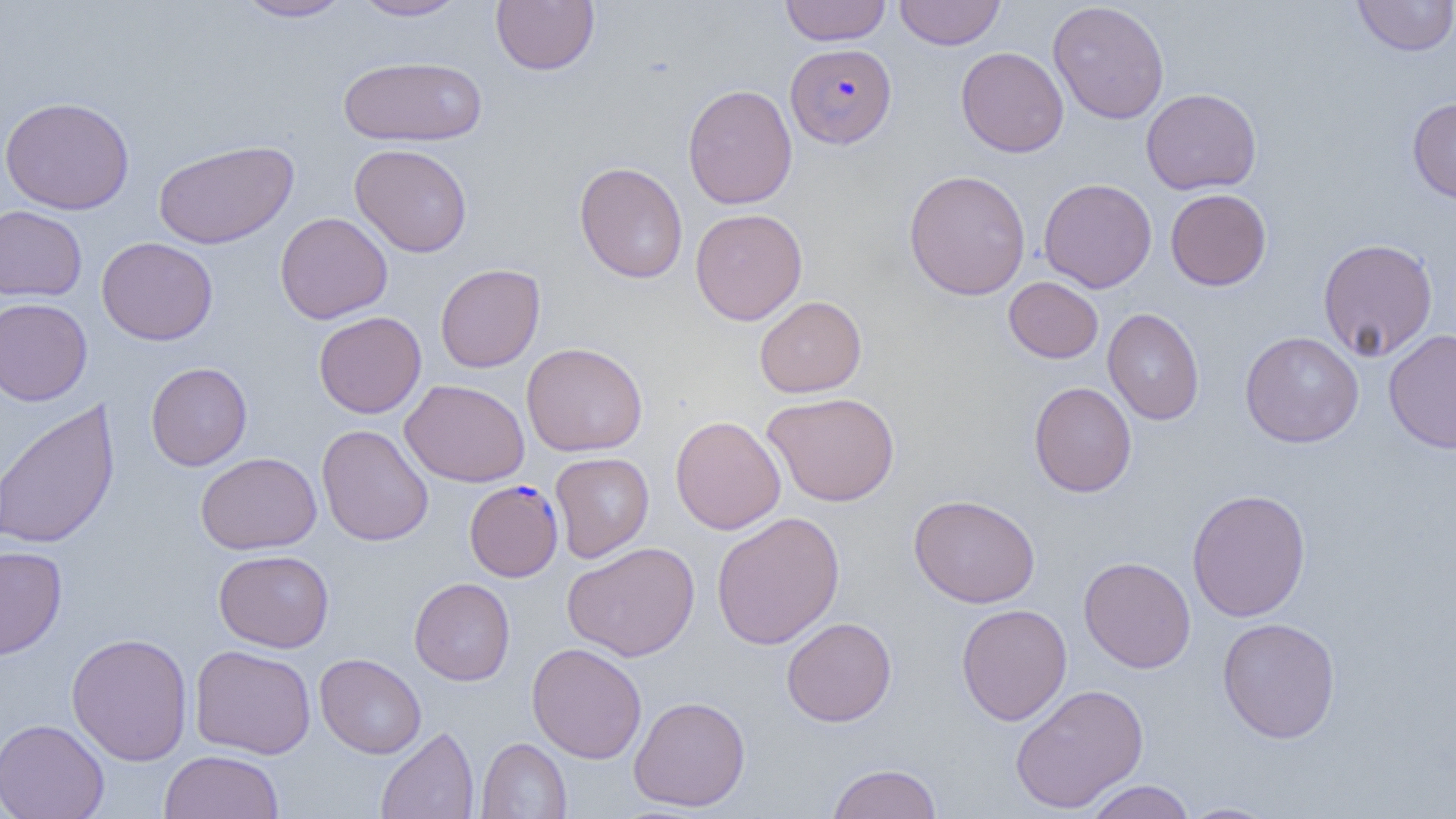

Summary:
  - Coordinate format: approximate bounding boxes as [x1, y1, x2, y2] in pixels
  - Plasmodium falciparum-infected red blood cell locations: [785, 43, 897, 148], [464, 479, 563, 581]
  - Uninfected red blood cell locations: [234, 0, 355, 22], [349, 0, 469, 21], [780, 0, 891, 46], [894, 0, 1006, 49], [1352, 0, 1456, 56], [491, 1, 599, 75], [1048, 2, 1169, 124], [955, 46, 1069, 157], [338, 55, 487, 146], [682, 83, 797, 210], [1141, 88, 1261, 195], [0, 96, 135, 214], [1407, 97, 1456, 204], [153, 139, 298, 249], [349, 143, 473, 257], [574, 161, 688, 283], [903, 169, 1031, 300], [1038, 178, 1157, 293], [1165, 188, 1271, 290], [0, 205, 87, 301], [690, 208, 807, 325], [275, 212, 393, 324], [96, 236, 218, 345], [1317, 238, 1438, 361], [435, 263, 545, 372], [1004, 276, 1104, 363], [754, 296, 867, 397], [0, 297, 92, 406], [1103, 308, 1205, 425], [313, 311, 427, 418], [1383, 328, 1456, 453], [1240, 330, 1364, 447], [521, 342, 648, 456], [146, 362, 252, 471], [400, 379, 530, 487], [1028, 381, 1137, 497], [762, 392, 901, 507], [1, 398, 120, 550], [670, 415, 786, 534], [317, 424, 433, 546], [195, 452, 322, 554], [550, 452, 654, 562], [1187, 489, 1311, 622], [909, 494, 1040, 608], [711, 511, 845, 649], [562, 541, 700, 662], [0, 546, 67, 660], [213, 549, 334, 653], [1079, 556, 1196, 672], [409, 577, 515, 685], [955, 604, 1072, 726], [781, 617, 897, 726], [1217, 617, 1341, 743], [66, 632, 193, 766], [526, 642, 647, 763], [190, 645, 317, 759], [314, 653, 427, 759], [1010, 684, 1149, 814], [629, 695, 750, 812], [0, 718, 109, 819], [375, 726, 479, 818], [476, 737, 571, 818], [159, 750, 284, 819], [826, 762, 942, 819], [1082, 780, 1197, 819], [1177, 801, 1283, 819]
  - Slide-level diagnosis: Plasmodium falciparum
  - Image size: 1456×819 pixels
  - Preparation: thin blood film
  - Magnification: 1000x
  - Modality: light microscopy
  - Field of view: single